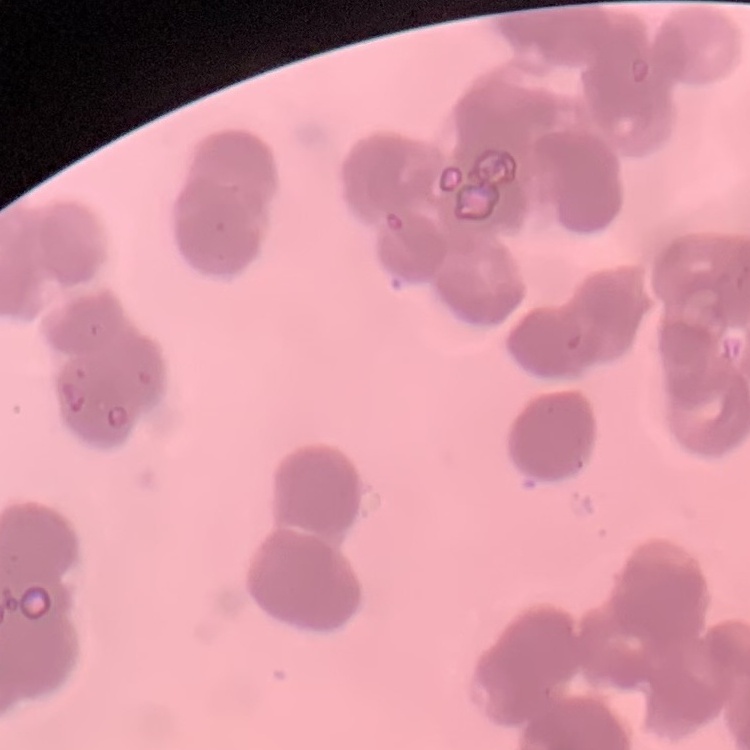

Summary:
  - Red blood cell morphology: rouleaux formation
  - Image type: one tile cut from a larger photomicrograph
  - Stain: Field's or Giemsa
  - Preparation: thin blood film